Locate every blood parasite and identify its species.
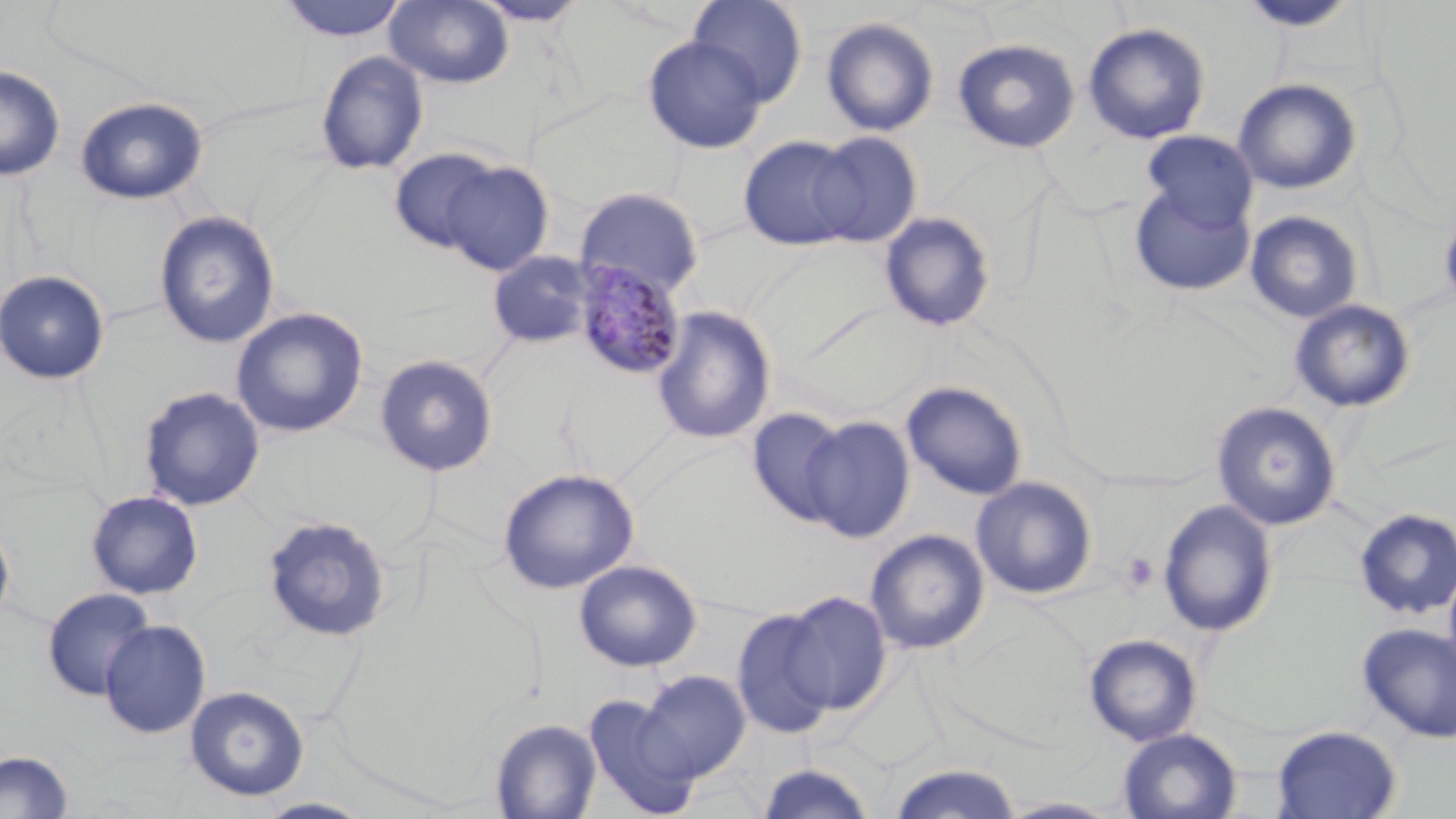
Approximate bounding boxes as (x1,y1)-(x2,y2) corner pairs in pixels.
Plasmodium malariae-infected red blood cells: (572,261)-(687,381).
No Plasmodium falciparum, Plasmodium ovale, Plasmodium vivax, Babesia divergens, or Trypanosoma brucei observed.

Summary:
  - Platelet locations: (1119,551)-(1159,594)
  - Uninfected red blood cell locations: (277,0)-(409,42), (384,0)-(514,88), (470,0)-(592,26), (688,0)-(808,106), (1237,0)-(1360,33), (821,17)-(939,137), (1082,23)-(1211,144), (642,35)-(768,155), (952,38)-(1081,153), (315,50)-(429,176), (0,65)-(65,181), (1232,78)-(1361,195), (75,97)-(208,205), (1142,131)-(1257,230), (808,132)-(923,247), (737,135)-(862,251), (388,147)-(505,255), (437,158)-(555,275), (1127,181)-(1255,297), (575,186)-(704,299), (1438,204)-(1456,318), (153,210)-(281,349), (1245,210)-(1364,324), (879,211)-(996,332), (488,250)-(596,348), (0,269)-(111,385), (1289,299)-(1416,413), (651,305)-(776,445), (231,307)-(369,438), (374,354)-(499,476), (901,381)-(1028,501), (138,386)-(265,511), (1211,401)-(1341,530), (746,408)-(853,528), (800,415)-(915,543), (497,467)-(639,595), (970,476)-(1097,599), (85,490)-(204,599), (1157,500)-(1277,637), (1354,507)-(1456,619), (262,515)-(393,643), (0,517)-(16,631), (865,529)-(989,654), (574,559)-(702,672), (1443,561)-(1456,681), (42,587)-(155,701), (778,590)-(892,717), (731,605)-(839,740), (99,619)-(212,739), (1357,623)-(1456,743), (1084,633)-(1202,746), (639,670)-(751,780), (184,685)-(309,801), (583,694)-(701,817), (490,718)-(602,819), (1271,725)-(1401,819), (1117,728)-(1241,818), (0,749)-(74,818), (756,761)-(877,819), (887,763)-(1023,819), (254,797)-(376,818), (997,797)-(1126,818)
  - Slide-level diagnosis: Plasmodium malariae
  - Field of view: single
  - Magnification: 1000x
  - Image size: 1456×819 pixels
  - Preparation: thin blood film
  - Stain: May-Grünwald-Giemsa
  - Modality: light microscopy